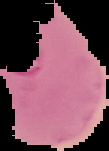
Summary:
  - Preparation: thin blood smear
  - Image size: 109×151 pixels
  - Image type: segmented cell region with the area outside set to black
  - Malaria status: parasitized